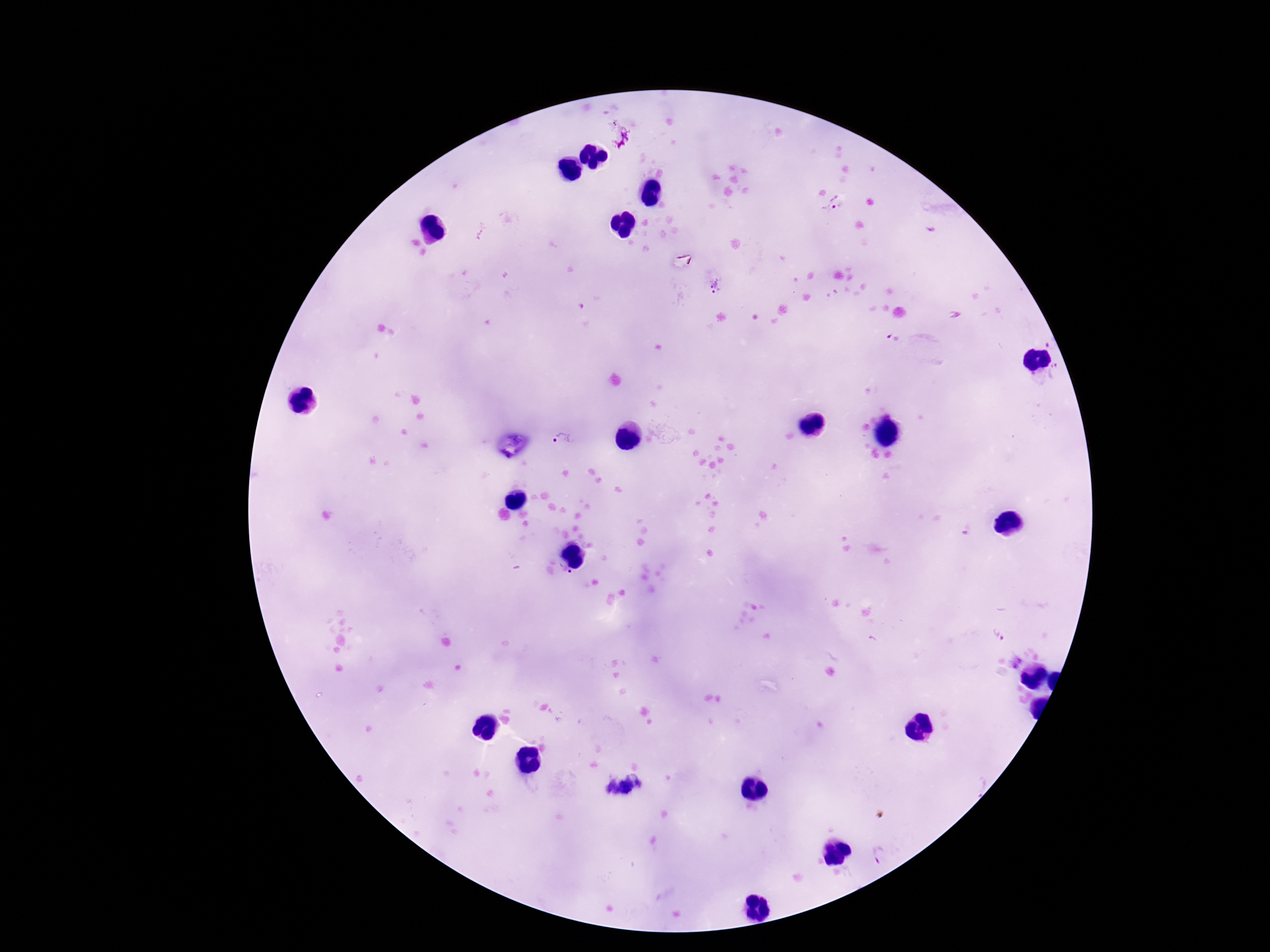
Approximate centers as {x, y} in pixels. Plasmodium parasite locations: {620, 136}, {834, 206}, {715, 286}, {893, 338}, {563, 441}, {565, 573}, {1000, 635}, {880, 854}. Giemsa stain. 100x magnification. Photographed through the microscope eyepiece with a smartphone camera. Thick blood film. One field from this slide. Patient malaria status: infected. Image is 1270×952 pixels.